Name the cell type shown.
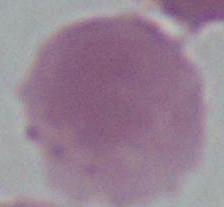
An erythrocyte.

Summary:
  - Modality: micrograph
  - Magnification: 1000x